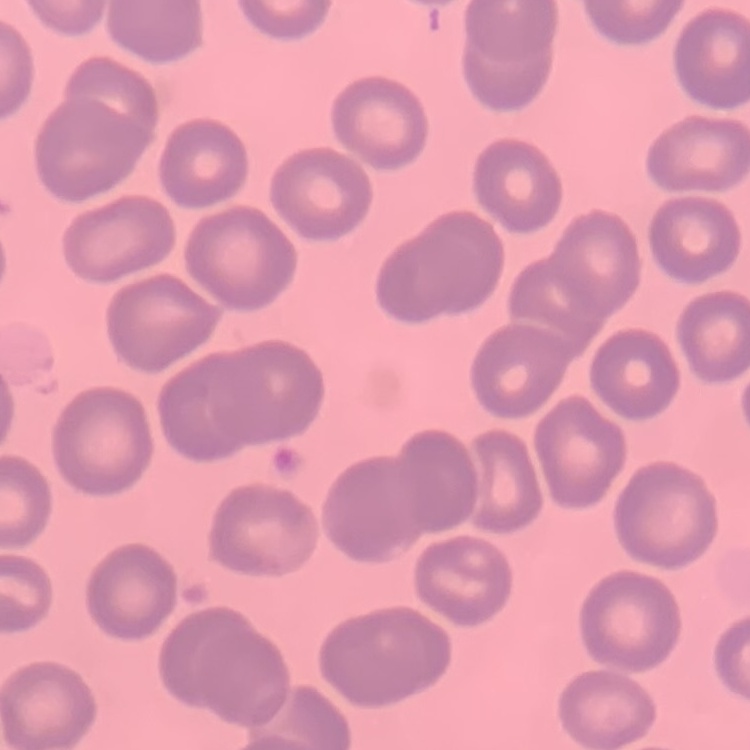

The red blood cells show no rouleaux formation. Field's or Giemsa stain. Square crop of a larger photomicrograph. Thin blood film.